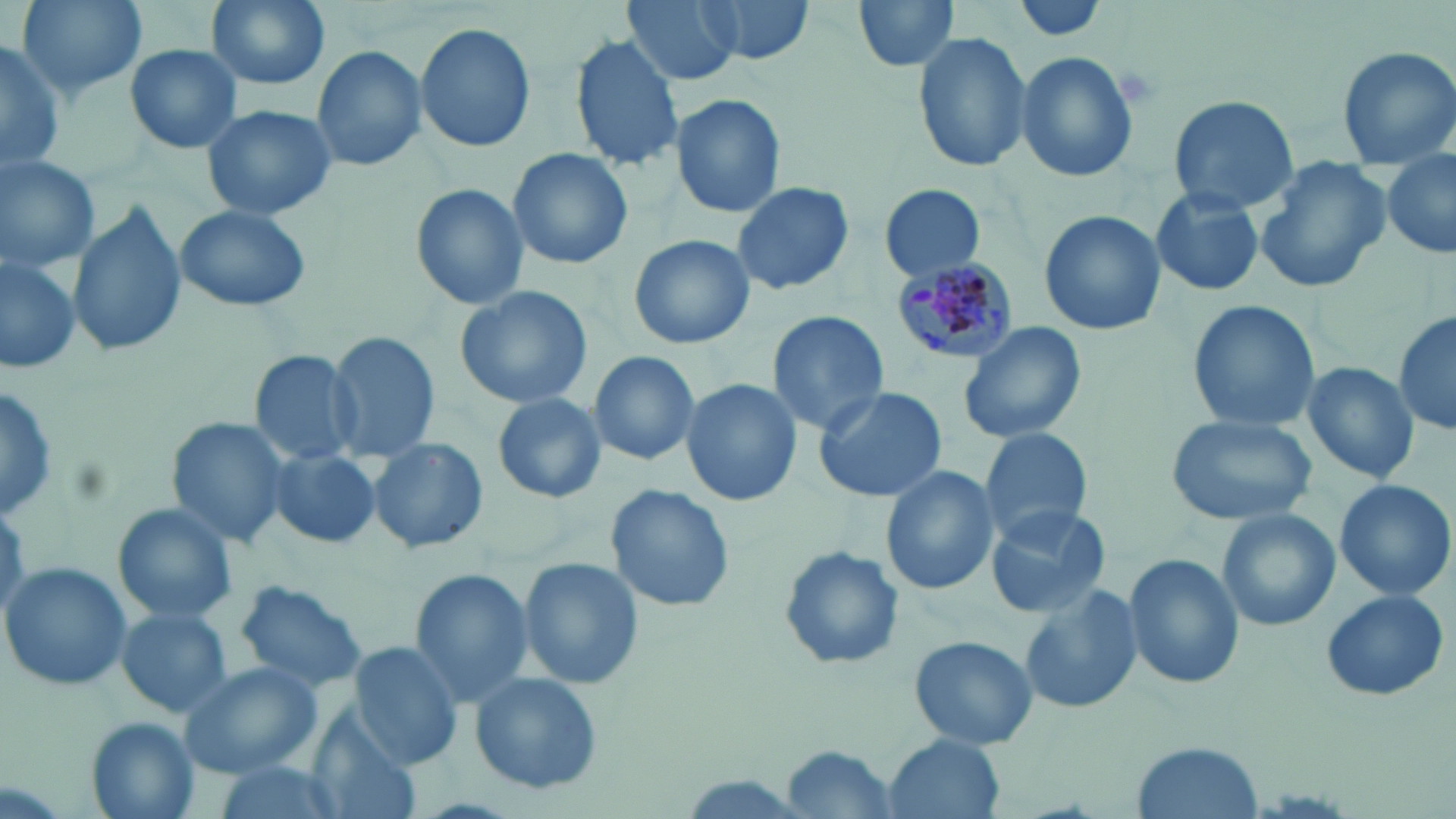 Approximate bounding boxes as (x1, y1, x2, y2) in pixels. Plasmodium malariae-infected red blood cell locations: (891, 255, 1020, 363). Uninfected red blood cell locations: (13, 0, 146, 102), (205, 0, 330, 91), (698, 0, 813, 66), (1013, 0, 1109, 44), (621, 1, 743, 87), (850, 1, 961, 76), (415, 22, 536, 152), (912, 29, 1030, 173), (569, 33, 684, 172), (0, 38, 65, 171), (125, 43, 242, 154), (312, 44, 428, 174), (1334, 44, 1456, 170), (1016, 51, 1139, 183), (669, 95, 786, 219), (1165, 95, 1300, 211), (201, 104, 338, 220), (507, 147, 633, 270), (0, 151, 101, 273), (1381, 151, 1456, 261), (1255, 158, 1392, 293), (733, 180, 855, 296), (408, 182, 529, 312), (880, 186, 986, 281), (1150, 187, 1267, 298), (69, 202, 185, 362), (173, 204, 313, 313), (1038, 211, 1164, 334), (629, 234, 754, 350), (0, 250, 83, 375), (453, 284, 592, 411), (1186, 299, 1320, 434), (1394, 308, 1456, 439), (768, 311, 889, 435), (957, 320, 1088, 445), (326, 332, 440, 465), (248, 349, 364, 465), (588, 351, 699, 466), (1298, 360, 1420, 485), (680, 379, 802, 506), (0, 385, 59, 524), (811, 387, 948, 503), (492, 392, 607, 503), (1166, 413, 1316, 528), (166, 415, 294, 548), (979, 426, 1094, 540), (367, 436, 488, 555), (265, 447, 382, 550), (880, 462, 997, 596), (1333, 477, 1455, 603), (606, 484, 735, 614), (113, 502, 238, 624), (987, 503, 1113, 620), (1217, 508, 1341, 633), (777, 543, 906, 672), (1123, 551, 1242, 691), (515, 557, 644, 689), (1, 561, 133, 691), (406, 568, 537, 708), (230, 579, 369, 695), (1020, 582, 1140, 717), (1318, 587, 1450, 702), (115, 608, 230, 718), (909, 635, 1035, 750), (349, 642, 465, 770), (178, 661, 323, 777), (469, 671, 604, 796), (305, 714, 421, 819), (82, 717, 199, 819), (882, 735, 1009, 819), (1132, 740, 1266, 819), (783, 746, 903, 817), (209, 762, 350, 819). Slide-level diagnosis: Plasmodium malariae. Image is 1456×819 pixels. One field of a larger specimen. Thin blood smear. Optical microscopy. May-Grünwald-Giemsa-stained preparation. 1000x magnification.